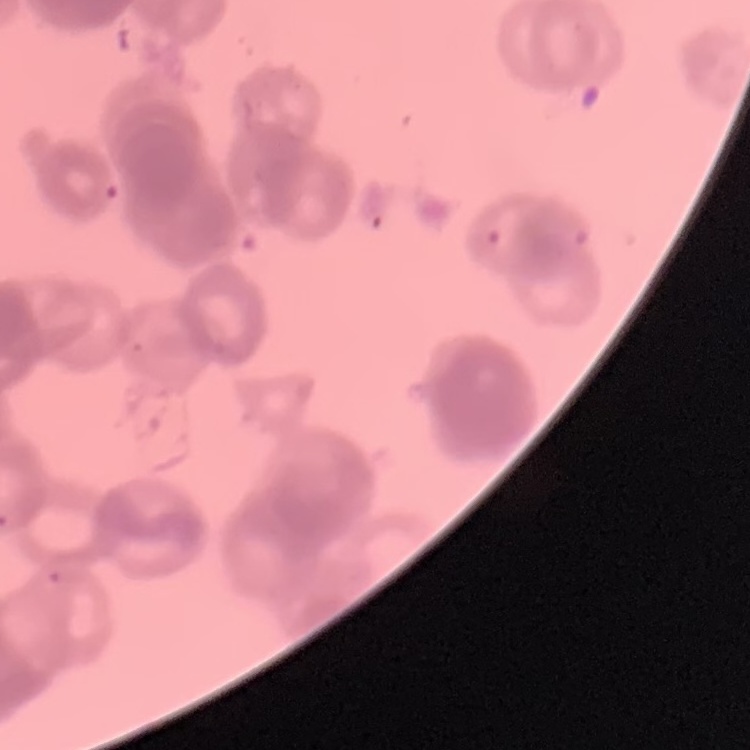

Summary:
  - Erythrocyte morphology: rouleaux formation
  - Preparation: thin blood smear
  - Image type: one tile cut from a larger photomicrograph
  - Stain: Field's or Giemsa